Give the extent of all Trypanosoma brucei.
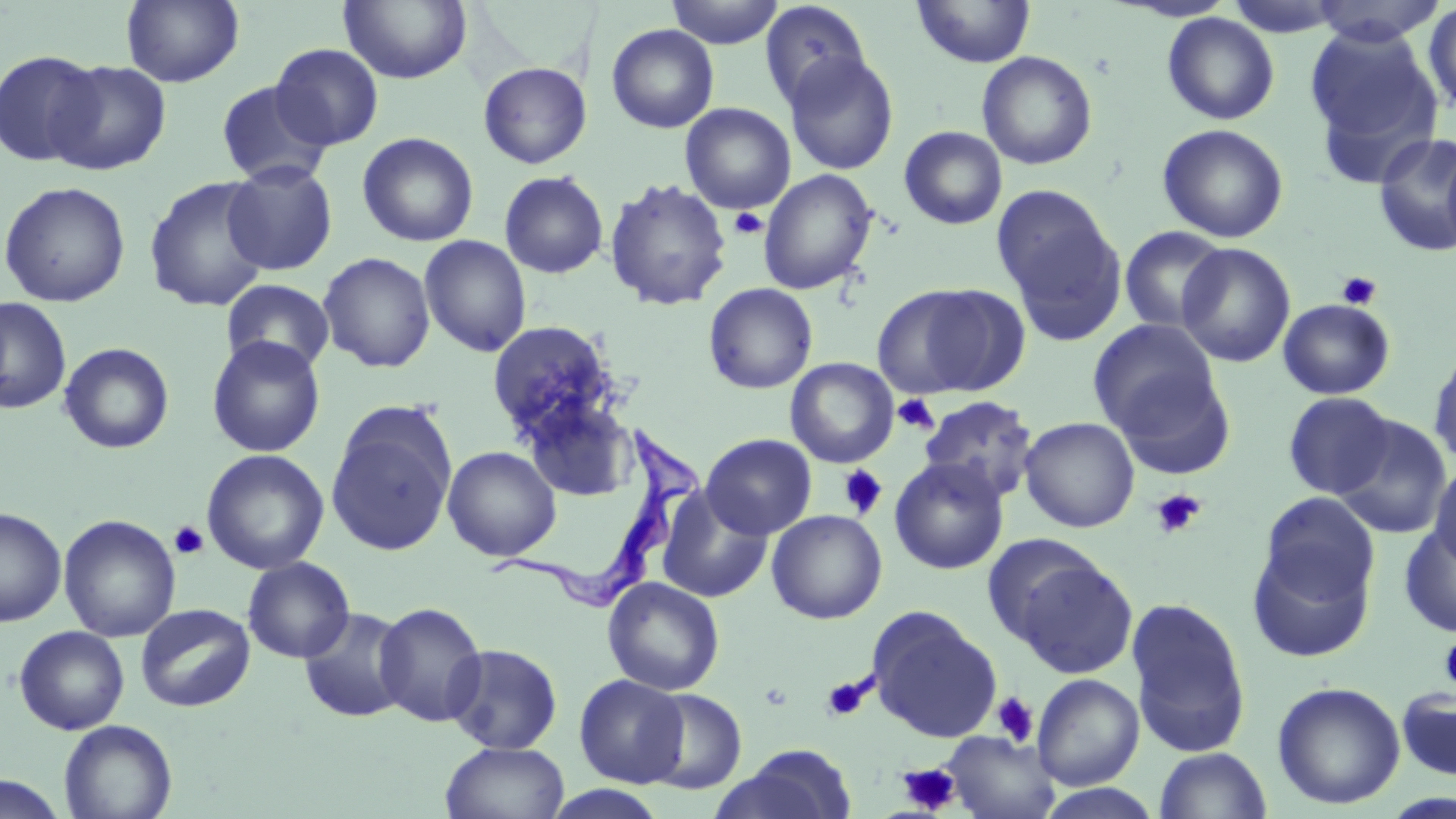
Approximate bounding boxes as (x1, y1, x2, y2) in pixels.
Trypanosoma brucei: (486, 424, 701, 613).

Summary:
  - Uninfected red blood cell locations: (122, 0, 244, 88), (338, 0, 472, 84), (665, 0, 785, 48), (758, 1, 872, 110), (911, 1, 1036, 69), (1304, 1, 1448, 46), (1422, 1, 1456, 119), (1161, 12, 1280, 125), (606, 23, 719, 133), (1305, 26, 1444, 178), (270, 43, 384, 150), (0, 49, 104, 167), (976, 51, 1098, 170), (784, 52, 899, 176), (48, 59, 170, 175), (478, 61, 591, 169), (215, 80, 333, 188), (680, 103, 796, 214), (1157, 123, 1289, 243), (899, 125, 1007, 229), (356, 131, 479, 247), (1373, 132, 1456, 257), (1442, 136, 1456, 259), (222, 161, 339, 276), (757, 169, 878, 295), (498, 170, 609, 279), (144, 176, 272, 313), (604, 177, 732, 312), (0, 181, 131, 307), (992, 185, 1125, 339), (1119, 225, 1230, 334), (419, 235, 532, 357), (1176, 242, 1296, 367), (318, 251, 436, 373), (221, 279, 335, 375), (703, 283, 818, 394), (872, 283, 1018, 400), (0, 297, 72, 414), (1278, 298, 1395, 399), (1087, 318, 1224, 441), (486, 320, 620, 445), (206, 336, 326, 457), (59, 342, 174, 453), (1427, 345, 1456, 469), (785, 358, 899, 468), (1110, 369, 1238, 479), (1282, 392, 1396, 499), (918, 395, 1038, 503), (519, 397, 639, 502), (326, 412, 456, 557), (1333, 414, 1452, 539), (1019, 416, 1140, 533), (701, 433, 817, 539), (443, 446, 561, 561), (201, 448, 329, 574), (889, 456, 1009, 575), (1429, 460, 1456, 571), (656, 486, 773, 603), (1258, 491, 1380, 606), (0, 506, 67, 627), (766, 510, 887, 624), (59, 514, 181, 642), (1399, 521, 1456, 638), (1246, 541, 1375, 663), (999, 547, 1138, 679), (243, 557, 355, 663), (603, 577, 725, 696), (1125, 596, 1252, 757), (373, 601, 487, 726), (135, 603, 256, 712), (298, 606, 411, 723), (866, 606, 1002, 743), (14, 625, 130, 735), (443, 643, 564, 754), (1032, 673, 1144, 790), (574, 674, 689, 788), (1272, 681, 1406, 810), (1396, 686, 1456, 781), (640, 688, 747, 794), (59, 719, 177, 819), (943, 731, 1061, 819), (440, 741, 569, 819), (713, 745, 860, 819), (1154, 747, 1271, 819), (0, 774, 69, 818), (1032, 783, 1165, 818), (543, 785, 669, 819)
  - Platelet locations: (730, 208, 768, 238), (1336, 271, 1382, 310), (893, 394, 938, 434), (838, 465, 888, 518), (1151, 489, 1206, 539), (168, 521, 210, 560), (1439, 632, 1456, 696), (820, 675, 873, 723), (992, 692, 1039, 746), (897, 763, 962, 815)
  - Slide-level diagnosis: Trypanosoma brucei
  - Preparation: thin blood film
  - Magnification: 1000x
  - Field of view: one of a larger specimen
  - Modality: light microscopy
  - Image size: 1456×819 pixels
  - Stain: May-Grünwald-Giemsa